Identify the parasite.
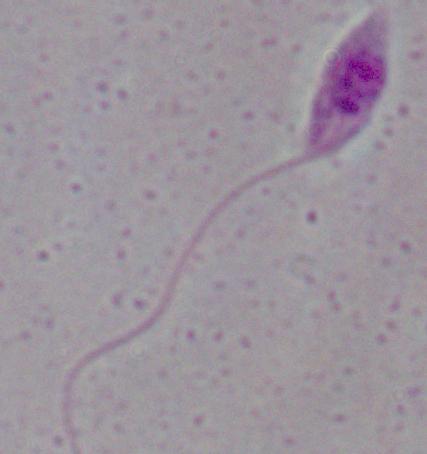

This is Leishmania.

Summary:
  - Magnification: 1000x
  - Modality: micrograph